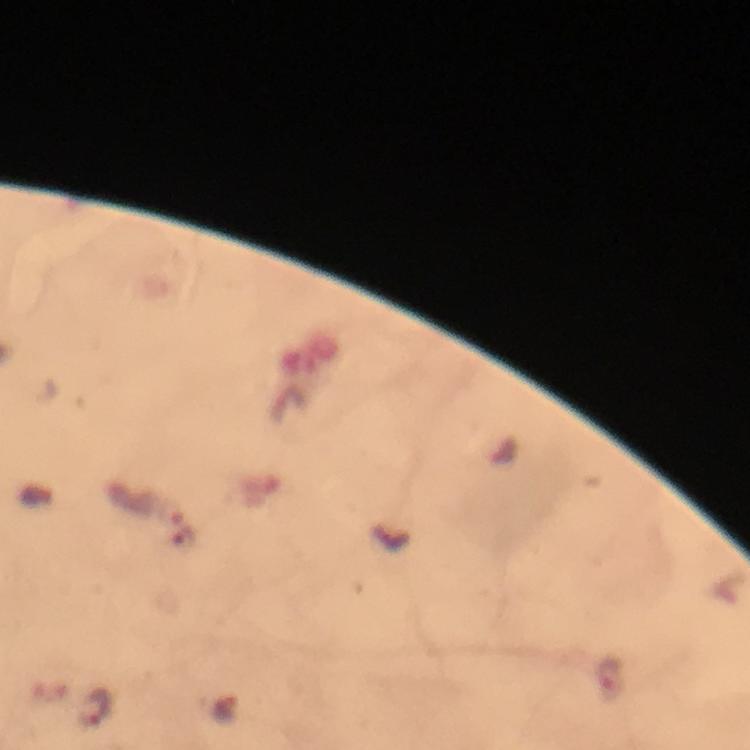
capture = smartphone photograph through a microscope
stain = Giemsa
preparation = thick blood smear
Plasmodium parasite locations = approximate centers as (x, y) in pixels: (611, 677), (95, 707)
context = from a diagnostic examination for malaria
image size = 750×750 pixels
immersion oil = applied
cropped from = one field of view
magnification = 100x